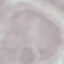

Summary:
  - Malaria status: uninfected
  - Capture: smartphone through the microscope eyepiece
  - Stain: Giemsa
  - Preparation: thin smear
  - Image type: cell patch, automatically extracted from a larger field of view and resized to 64 × 64 pixels